Outline each uninfected red blood cell.
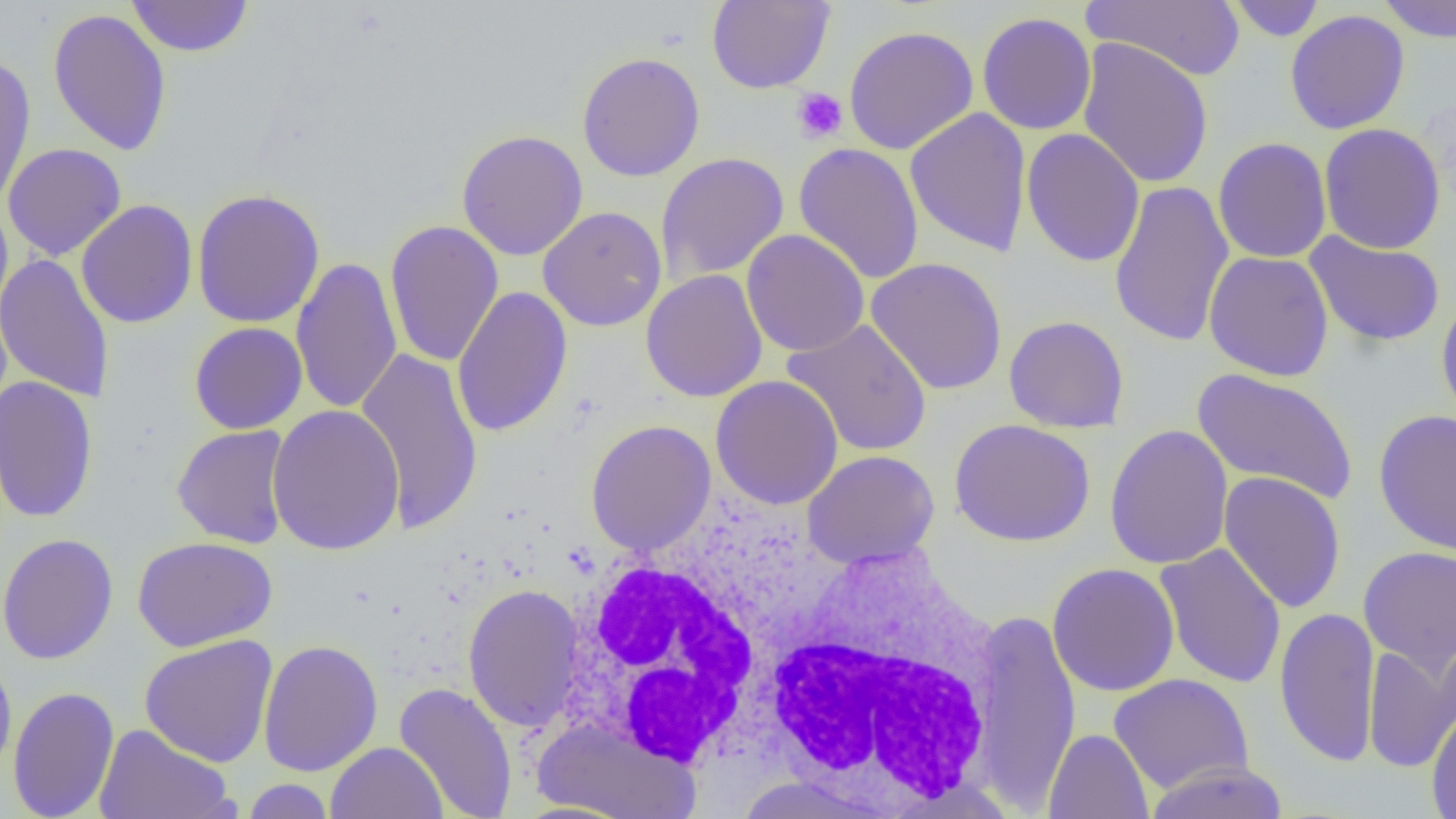
Approximate bounding boxes as named x1/y1/x2/y2 corners in pixels.
Uninfected red blood cells: (x1=125, y1=0, x2=254, y2=57), (x1=706, y1=0, x2=835, y2=93), (x1=1083, y1=0, x2=1246, y2=82), (x1=1225, y1=0, x2=1327, y2=41), (x1=1374, y1=0, x2=1456, y2=42), (x1=48, y1=7, x2=172, y2=156), (x1=1285, y1=9, x2=1410, y2=135), (x1=976, y1=12, x2=1097, y2=135), (x1=843, y1=25, x2=979, y2=155), (x1=1076, y1=37, x2=1214, y2=189), (x1=576, y1=51, x2=705, y2=182), (x1=0, y1=54, x2=36, y2=209), (x1=904, y1=107, x2=1033, y2=257), (x1=1318, y1=123, x2=1446, y2=255), (x1=1021, y1=128, x2=1145, y2=267), (x1=456, y1=129, x2=589, y2=261), (x1=1213, y1=137, x2=1332, y2=264), (x1=793, y1=142, x2=924, y2=284), (x1=3, y1=143, x2=127, y2=261), (x1=656, y1=152, x2=790, y2=284), (x1=40, y1=170, x2=160, y2=309), (x1=1108, y1=180, x2=1235, y2=348), (x1=191, y1=188, x2=325, y2=329), (x1=76, y1=199, x2=198, y2=329), (x1=0, y1=200, x2=13, y2=325), (x1=538, y1=206, x2=667, y2=331), (x1=385, y1=221, x2=504, y2=367), (x1=741, y1=229, x2=869, y2=357), (x1=1304, y1=232, x2=1445, y2=347), (x1=1203, y1=251, x2=1334, y2=382), (x1=0, y1=253, x2=115, y2=405), (x1=290, y1=256, x2=403, y2=415), (x1=865, y1=257, x2=1008, y2=396), (x1=640, y1=269, x2=768, y2=403), (x1=451, y1=286, x2=574, y2=437), (x1=1435, y1=291, x2=1456, y2=428), (x1=1004, y1=315, x2=1130, y2=433), (x1=782, y1=318, x2=933, y2=458), (x1=189, y1=322, x2=308, y2=435), (x1=355, y1=345, x2=485, y2=537), (x1=1191, y1=367, x2=1358, y2=504), (x1=0, y1=375, x2=99, y2=524), (x1=710, y1=375, x2=843, y2=510), (x1=266, y1=403, x2=405, y2=556), (x1=1373, y1=409, x2=1456, y2=556), (x1=949, y1=418, x2=1096, y2=547), (x1=586, y1=419, x2=716, y2=556), (x1=171, y1=424, x2=293, y2=549), (x1=1104, y1=424, x2=1234, y2=570), (x1=802, y1=450, x2=940, y2=570), (x1=1218, y1=471, x2=1347, y2=614), (x1=0, y1=533, x2=118, y2=665), (x1=131, y1=536, x2=277, y2=652), (x1=1154, y1=542, x2=1287, y2=689), (x1=1358, y1=546, x2=1456, y2=675), (x1=1047, y1=562, x2=1180, y2=697), (x1=463, y1=583, x2=584, y2=733), (x1=1274, y1=606, x2=1380, y2=767), (x1=970, y1=608, x2=1082, y2=811), (x1=139, y1=634, x2=278, y2=767), (x1=257, y1=639, x2=384, y2=776), (x1=1363, y1=642, x2=1456, y2=772), (x1=0, y1=651, x2=18, y2=780), (x1=1108, y1=673, x2=1255, y2=794), (x1=394, y1=682, x2=518, y2=818), (x1=7, y1=685, x2=120, y2=819), (x1=1425, y1=707, x2=1456, y2=819), (x1=532, y1=718, x2=701, y2=819), (x1=94, y1=724, x2=235, y2=819), (x1=1043, y1=728, x2=1154, y2=819), (x1=326, y1=741, x2=447, y2=819), (x1=1143, y1=759, x2=1291, y2=819), (x1=730, y1=775, x2=890, y2=818), (x1=240, y1=779, x2=336, y2=818).

slide_level_diagnosis: negative for blood parasites
white_blood_cell_locations: 'approximate bounding boxes as named x1/y1/x2/y2 corners in pixels: (x1=556, y1=535, x2=795, y2=768), (x1=757, y1=545, x2=1008, y2=809)'
magnification: 1000x
field_of_view: single
platelet_locations: 'approximate bounding boxes as named x1/y1/x2/y2 corners in pixels: (x1=791, y1=88, x2=848, y2=143)'
preparation: thin blood film
modality: optical microscopy
image_size: 1456×819 pixels